Report the malaria status of this cell.
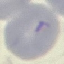
Uninfected.

Giemsa stain. Acquired by smartphone through the microscope eyepiece. Thin blood film. Automatically extracted cell patch, resized to 64 × 64 pixels.